Comment on the morphology of the erythrocytes.
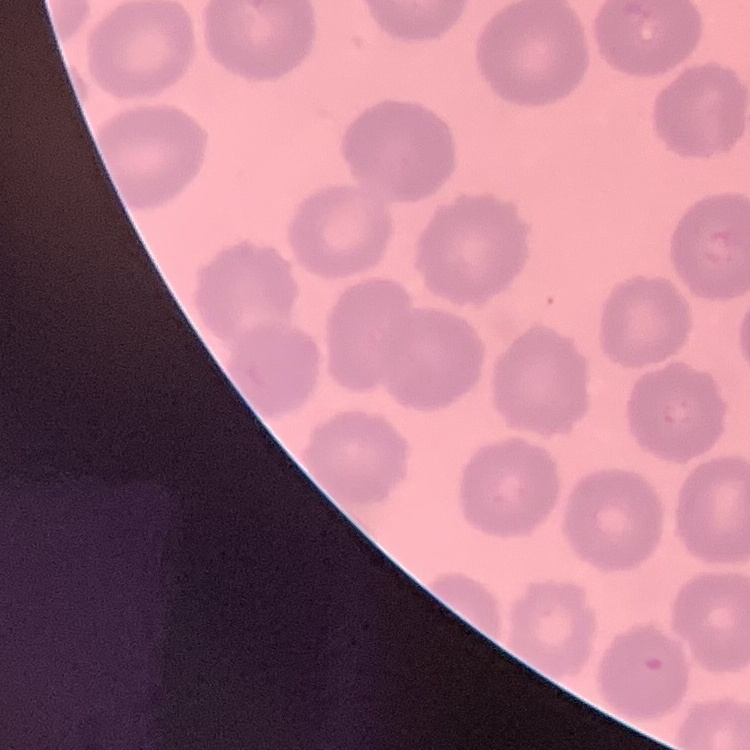

They show no rouleaux formation.

image type = square crop of a larger photomicrograph
stain = Field's or Giemsa
preparation = thin peripheral smear